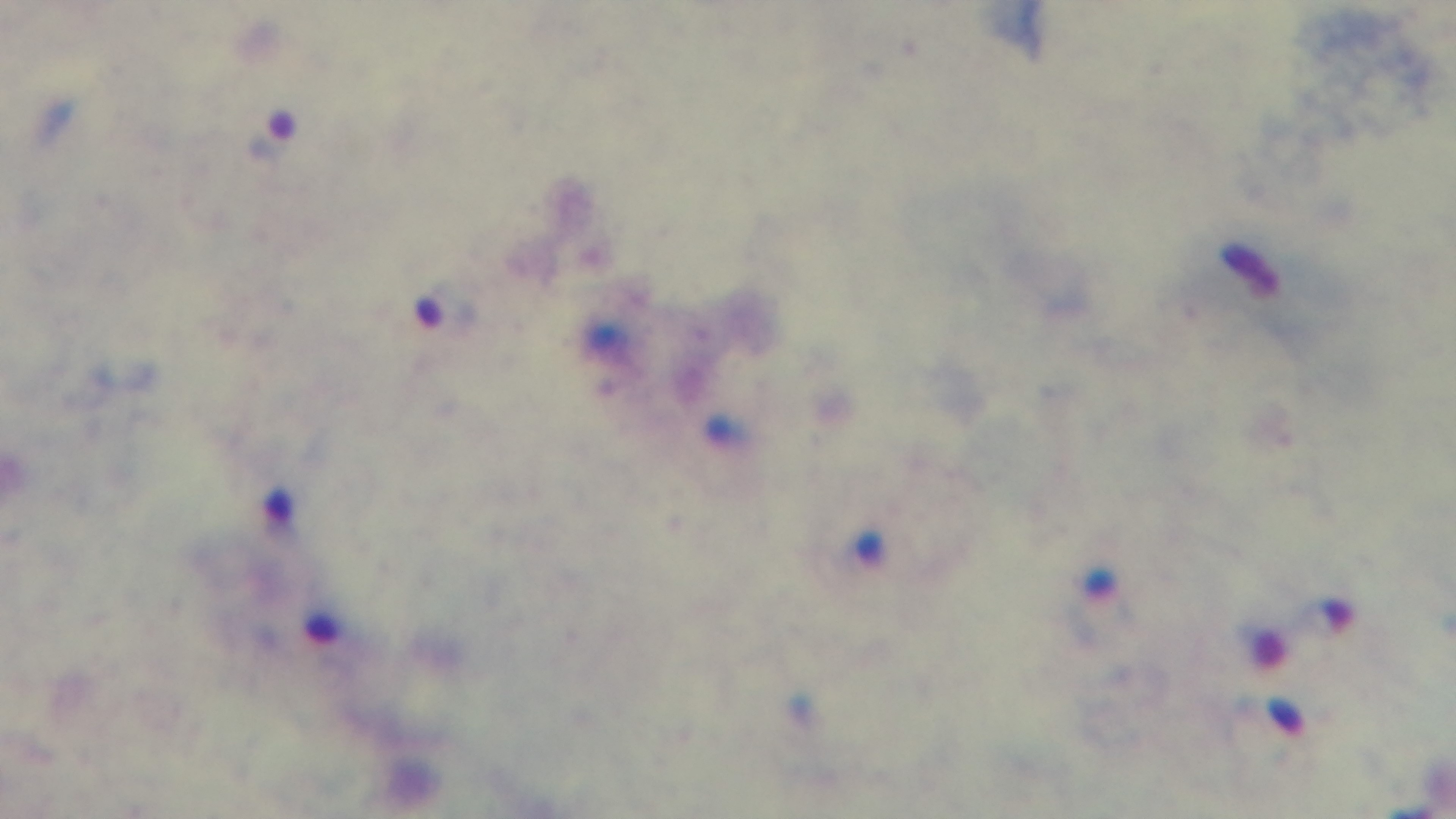

stain: Giemsa
preparation: thick blood film
malaria_status: infected
field_of_view: single
capture: mounted 4K digital camera
objective: 100x oil immersion
modality: light microscopy